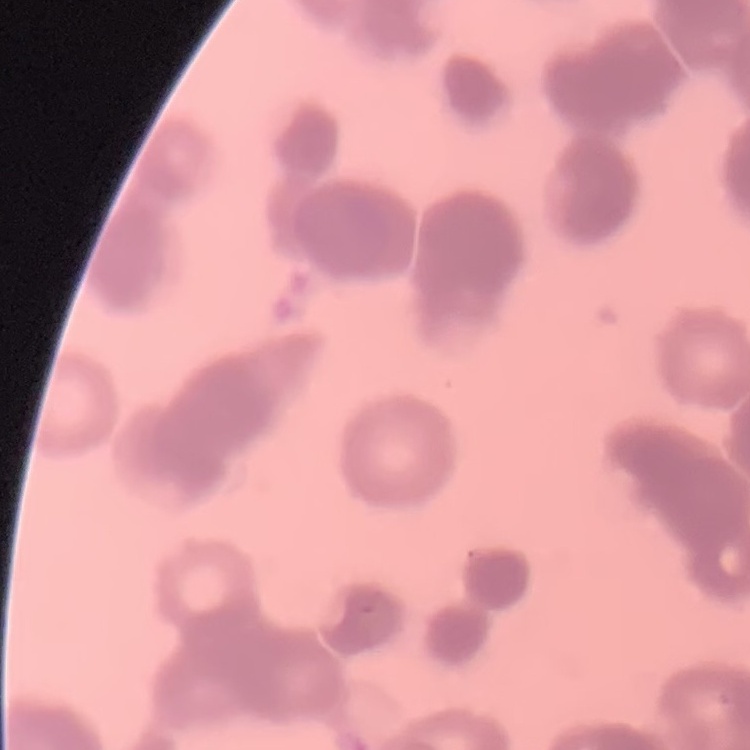

Summary:
  - Erythrocyte morphology: rouleaux formation
  - Stain: Field's or Giemsa
  - Preparation: thin blood smear
  - Image type: one tile cut from a larger photomicrograph